Identify the parasite.
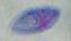
Toxoplasma gondii.

Summary:
  - Magnification: 1000x
  - Modality: photomicrograph